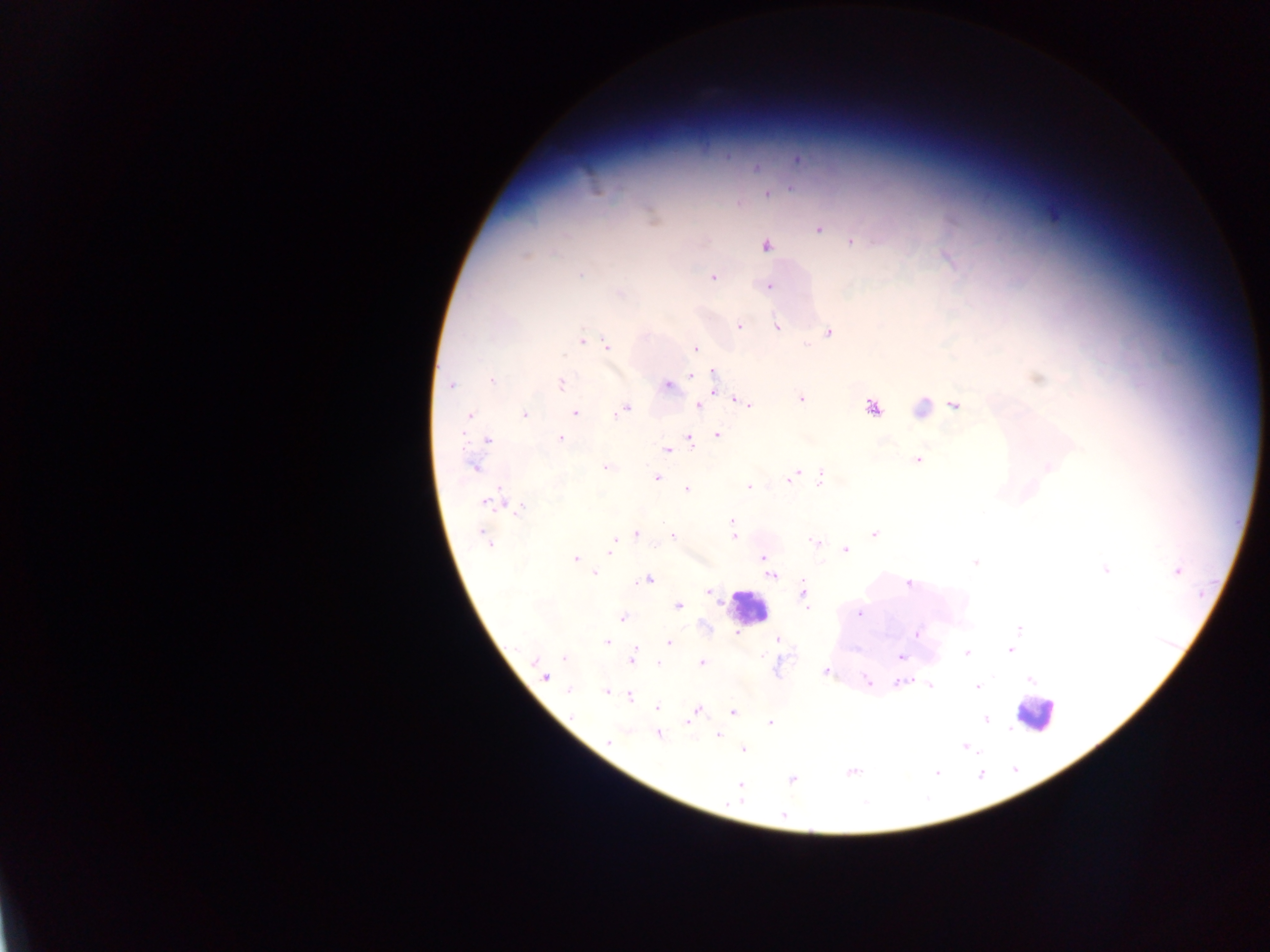

{
  "preparation": "thick blood smear",
  "leukocyte_locations": "approximate centers as x y in pixels: 746 607; 1034 713",
  "image_size": "1270×952 pixels",
  "country": "Ghana",
  "plasmodium_parasite_locations": "approximate centers as x y in pixels: 797 159; 756 167; 768 194; 818 229; 852 242; 766 246; 948 258; 581 274; 713 277; 767 286; 620 293; 739 326; 777 326; 828 332; 582 341; 590 342; 607 345; 696 348; 693 374; 713 375; 1037 378; 492 380; 561 383; 451 385; 669 386; 801 398; 744 403; 699 405; 955 405; 872 408; 921 408; 623 410; 574 412; 525 414; 470 415; 718 435; 561 438; 488 440; 690 440; 667 450; 918 459; 474 467; 1049 467; 606 468; 792 476; 656 478; 821 478; 748 486; 687 490; 490 502; 519 509; 732 523; 637 533; 874 533; 733 534; 673 536; 485 539; 814 541; 611 546; 846 549; 764 557; 575 558; 975 562; 1106 569; 1176 571; 594 573; 771 575; 648 580; 909 584; 709 592; 803 594; 806 600; 678 605; 807 608; 860 613; 622 618; 1018 629; 737 632; 917 634; 778 639; 607 642; 669 642; 1010 650; 967 653; 564 657; 900 657; 632 658; 702 663; 660 664; 825 671; 545 675; 1030 679; 867 681; 898 683; 930 685; 977 688; 569 690; 605 691; 630 696; 658 708; 698 710; 732 712; 693 716; 986 719; 688 722; 770 723; 658 735; 718 735; 609 740; 965 746; 743 750; 852 771; 937 773; 792 779; 740 786; 784 815",
  "capture": "mobile-phone photograph through a microscope",
  "field_of_view": "single"
}